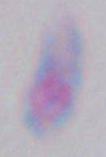

Summary:
  - Identification: Toxoplasma gondii
  - Magnification: 1000x
  - Modality: photomicrograph